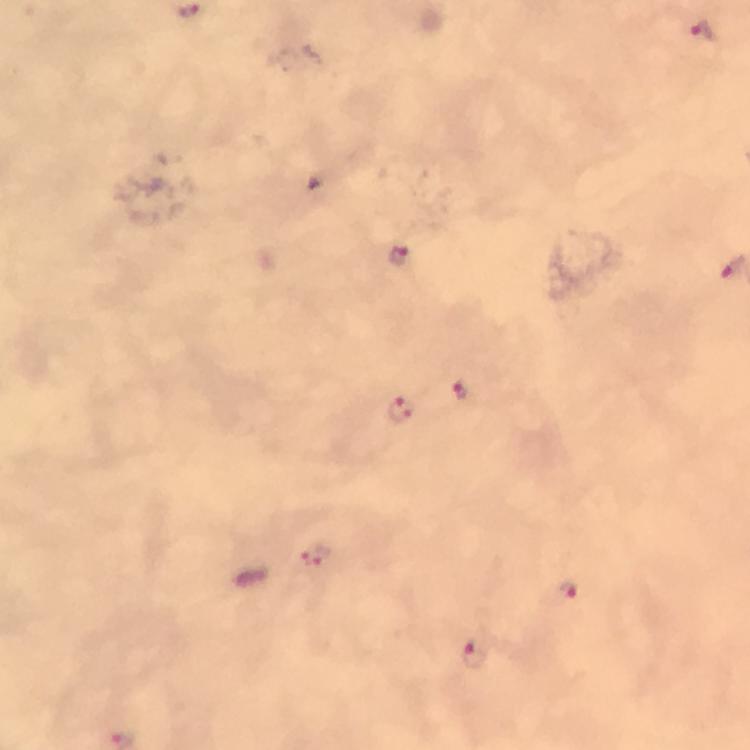

malaria_parasite_locations: 'approximate object centers, in pixels from the top-left corner: (x=704, y=33), (x=400, y=259), (x=462, y=392), (x=397, y=410), (x=316, y=556), (x=567, y=590), (x=474, y=654)'
capture: smartphone mounted on the microscope
stain: Giemsa
magnification: 100x
preparation: thick blood smear
context: from a diagnostic examination for malaria
cropped_from: one field of view
immersion_oil: used
image_size: 750×750 pixels